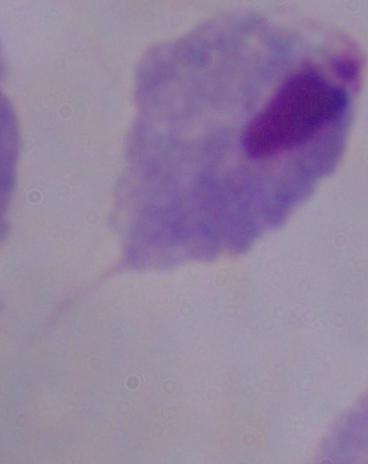
A trichomonad is seen. Photomicrograph. Captured at 1000x magnification.